Name the parasite shown.
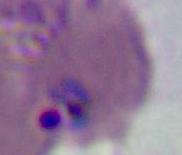
This is Plasmodium.

{
  "magnification": "400x or 1000x",
  "modality": "micrograph"
}